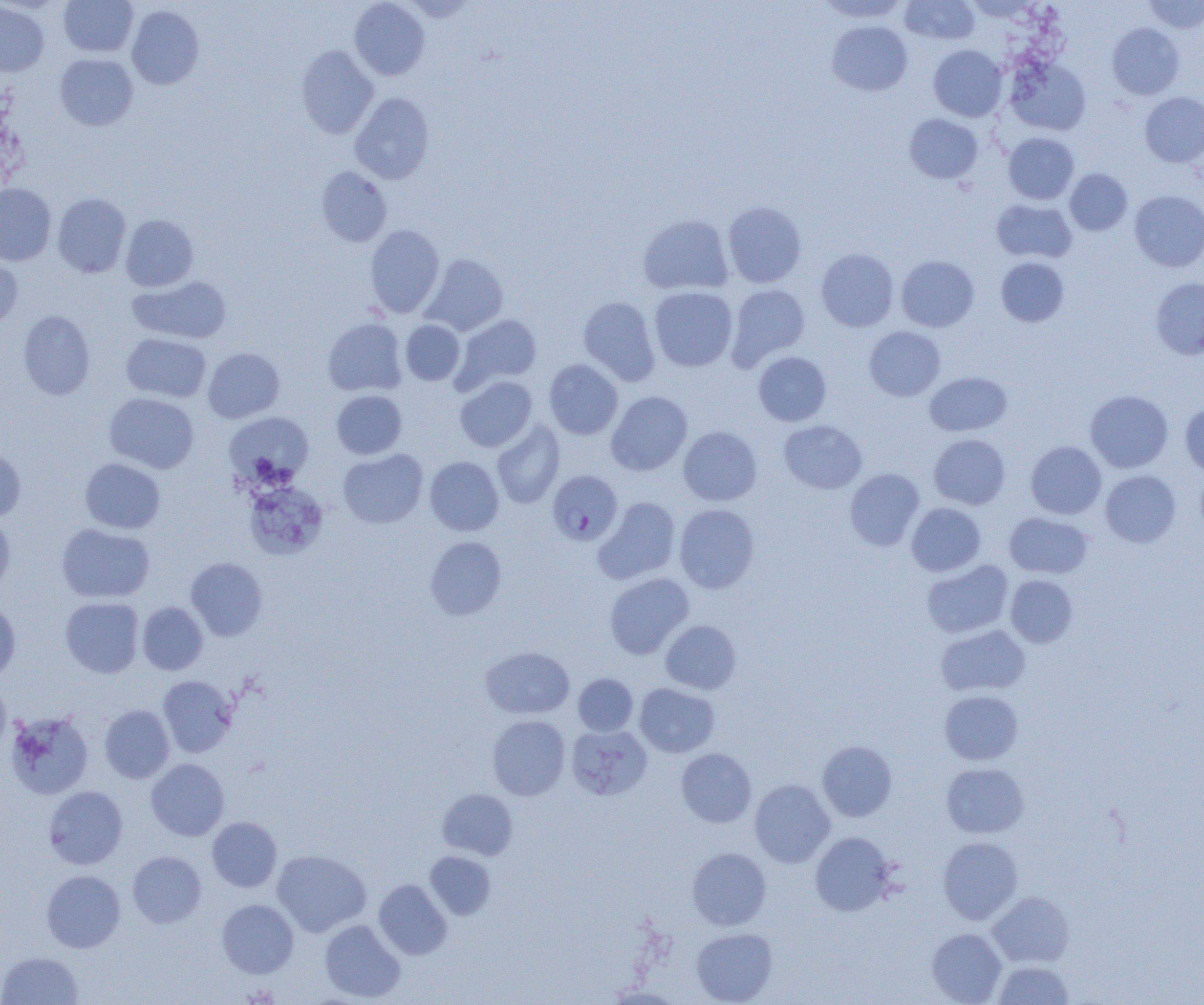
Summary:
  - Coordinate format: approximate bounding boxes as named x1/y1/x2/y2 corners in pixels
  - Uninfected red blood cell locations: (x1=58, y1=0, x2=138, y2=57), (x1=349, y1=0, x2=430, y2=80), (x1=403, y1=0, x2=478, y2=23), (x1=815, y1=0, x2=909, y2=23), (x1=900, y1=0, x2=980, y2=46), (x1=1144, y1=0, x2=1204, y2=34), (x1=0, y1=2, x2=49, y2=76), (x1=126, y1=5, x2=204, y2=89), (x1=827, y1=21, x2=912, y2=95), (x1=1108, y1=23, x2=1184, y2=100), (x1=295, y1=45, x2=378, y2=138), (x1=928, y1=45, x2=1007, y2=121), (x1=55, y1=53, x2=138, y2=131), (x1=1006, y1=57, x2=1091, y2=136), (x1=350, y1=92, x2=435, y2=184), (x1=1140, y1=92, x2=1204, y2=167), (x1=904, y1=113, x2=983, y2=183), (x1=1003, y1=133, x2=1079, y2=204), (x1=316, y1=167, x2=392, y2=247), (x1=1065, y1=168, x2=1132, y2=235), (x1=0, y1=183, x2=56, y2=266), (x1=1130, y1=190, x2=1204, y2=272), (x1=52, y1=193, x2=131, y2=278), (x1=991, y1=199, x2=1077, y2=263), (x1=723, y1=200, x2=806, y2=288), (x1=638, y1=213, x2=734, y2=295), (x1=121, y1=214, x2=199, y2=291), (x1=365, y1=224, x2=444, y2=317), (x1=816, y1=248, x2=899, y2=332), (x1=421, y1=253, x2=508, y2=336), (x1=0, y1=254, x2=23, y2=330), (x1=896, y1=255, x2=979, y2=332), (x1=996, y1=257, x2=1069, y2=327), (x1=128, y1=276, x2=232, y2=344), (x1=1151, y1=278, x2=1204, y2=360), (x1=727, y1=284, x2=810, y2=369), (x1=649, y1=287, x2=738, y2=372), (x1=578, y1=297, x2=660, y2=385), (x1=18, y1=310, x2=95, y2=400), (x1=454, y1=314, x2=542, y2=392), (x1=323, y1=317, x2=407, y2=396), (x1=400, y1=320, x2=465, y2=385), (x1=864, y1=326, x2=946, y2=401), (x1=121, y1=333, x2=211, y2=403), (x1=203, y1=347, x2=284, y2=423), (x1=753, y1=351, x2=831, y2=426), (x1=544, y1=359, x2=623, y2=439), (x1=925, y1=372, x2=1012, y2=436), (x1=455, y1=376, x2=537, y2=452), (x1=1085, y1=389, x2=1173, y2=473), (x1=331, y1=390, x2=407, y2=459), (x1=606, y1=391, x2=693, y2=476), (x1=104, y1=392, x2=199, y2=474), (x1=1180, y1=403, x2=1204, y2=477), (x1=224, y1=411, x2=314, y2=488), (x1=779, y1=420, x2=867, y2=494), (x1=492, y1=421, x2=565, y2=508), (x1=678, y1=426, x2=761, y2=505), (x1=929, y1=434, x2=1010, y2=509), (x1=1026, y1=441, x2=1106, y2=519), (x1=0, y1=447, x2=26, y2=522), (x1=338, y1=449, x2=427, y2=528), (x1=424, y1=456, x2=504, y2=536), (x1=80, y1=458, x2=165, y2=534), (x1=844, y1=468, x2=924, y2=550), (x1=1100, y1=470, x2=1181, y2=547), (x1=1195, y1=470, x2=1204, y2=540), (x1=246, y1=482, x2=328, y2=559), (x1=593, y1=497, x2=681, y2=584), (x1=906, y1=502, x2=986, y2=576), (x1=674, y1=503, x2=759, y2=593), (x1=0, y1=512, x2=15, y2=595), (x1=1004, y1=512, x2=1093, y2=579), (x1=56, y1=523, x2=155, y2=603), (x1=425, y1=536, x2=507, y2=620), (x1=185, y1=558, x2=267, y2=641), (x1=921, y1=560, x2=1013, y2=638), (x1=604, y1=573, x2=694, y2=659), (x1=1006, y1=575, x2=1078, y2=648), (x1=60, y1=597, x2=144, y2=677), (x1=0, y1=598, x2=21, y2=684), (x1=137, y1=602, x2=208, y2=675), (x1=661, y1=620, x2=741, y2=694), (x1=935, y1=624, x2=1030, y2=696), (x1=481, y1=646, x2=574, y2=719), (x1=573, y1=673, x2=638, y2=736), (x1=158, y1=675, x2=238, y2=757), (x1=0, y1=680, x2=11, y2=759), (x1=634, y1=683, x2=719, y2=757), (x1=939, y1=690, x2=1023, y2=765), (x1=99, y1=705, x2=175, y2=783), (x1=5, y1=710, x2=94, y2=800), (x1=487, y1=715, x2=570, y2=800), (x1=566, y1=724, x2=652, y2=800), (x1=817, y1=741, x2=897, y2=821), (x1=676, y1=748, x2=756, y2=827), (x1=146, y1=758, x2=229, y2=841), (x1=942, y1=763, x2=1029, y2=838), (x1=750, y1=779, x2=835, y2=867), (x1=44, y1=785, x2=128, y2=869), (x1=438, y1=788, x2=518, y2=860), (x1=206, y1=817, x2=282, y2=892), (x1=810, y1=831, x2=896, y2=916), (x1=938, y1=836, x2=1023, y2=925), (x1=687, y1=847, x2=771, y2=930), (x1=272, y1=849, x2=371, y2=937), (x1=127, y1=851, x2=206, y2=928), (x1=425, y1=851, x2=496, y2=920), (x1=41, y1=870, x2=125, y2=953), (x1=374, y1=879, x2=452, y2=960), (x1=987, y1=891, x2=1075, y2=967), (x1=217, y1=899, x2=299, y2=978), (x1=319, y1=919, x2=405, y2=1002), (x1=691, y1=927, x2=777, y2=1004), (x1=926, y1=928, x2=1007, y2=1004), (x1=0, y1=951, x2=83, y2=1005), (x1=991, y1=959, x2=1075, y2=1004), (x1=604, y1=985, x2=684, y2=1004)
  - Plasmodium falciparum-infected red blood cell locations: (x1=547, y1=470, x2=622, y2=546)
  - Slide-level diagnosis: Plasmodium falciparum
  - Image size: 1204×1005 pixels
  - Field of view: one of a larger specimen
  - Modality: optical microscopy
  - Magnification: 1000x
  - Preparation: thin blood film